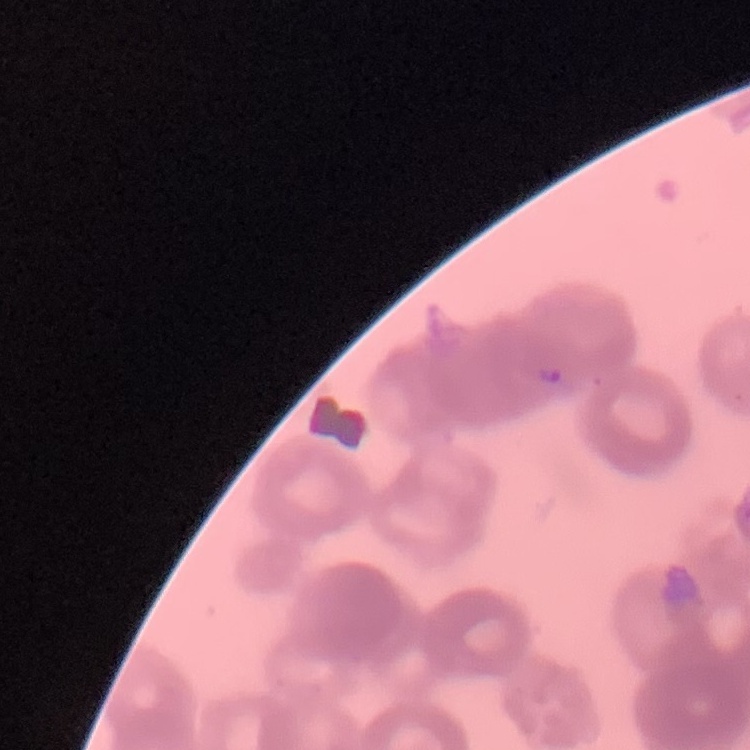
Summary:
  - Red blood cell morphology: rouleaux formation
  - Image type: one tile cut from a larger photomicrograph
  - Stain: Field's or Giemsa
  - Preparation: thin blood film